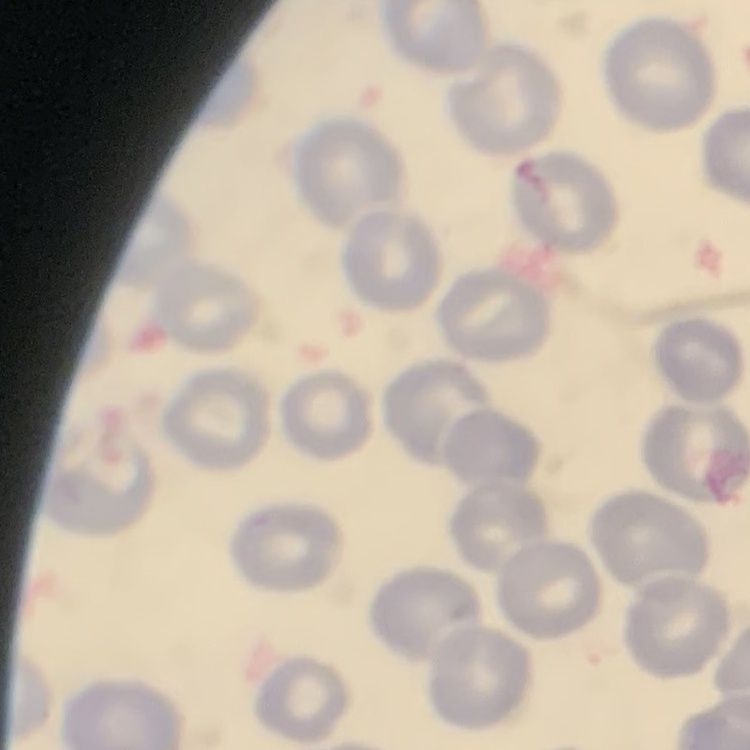

{
  "red_blood_cell_morphology": "no rouleaux formation",
  "image_type": "one tile cut from a larger photomicrograph",
  "stain": "Field's or Giemsa",
  "preparation": "thin blood film"
}